Name the blood parasite species.
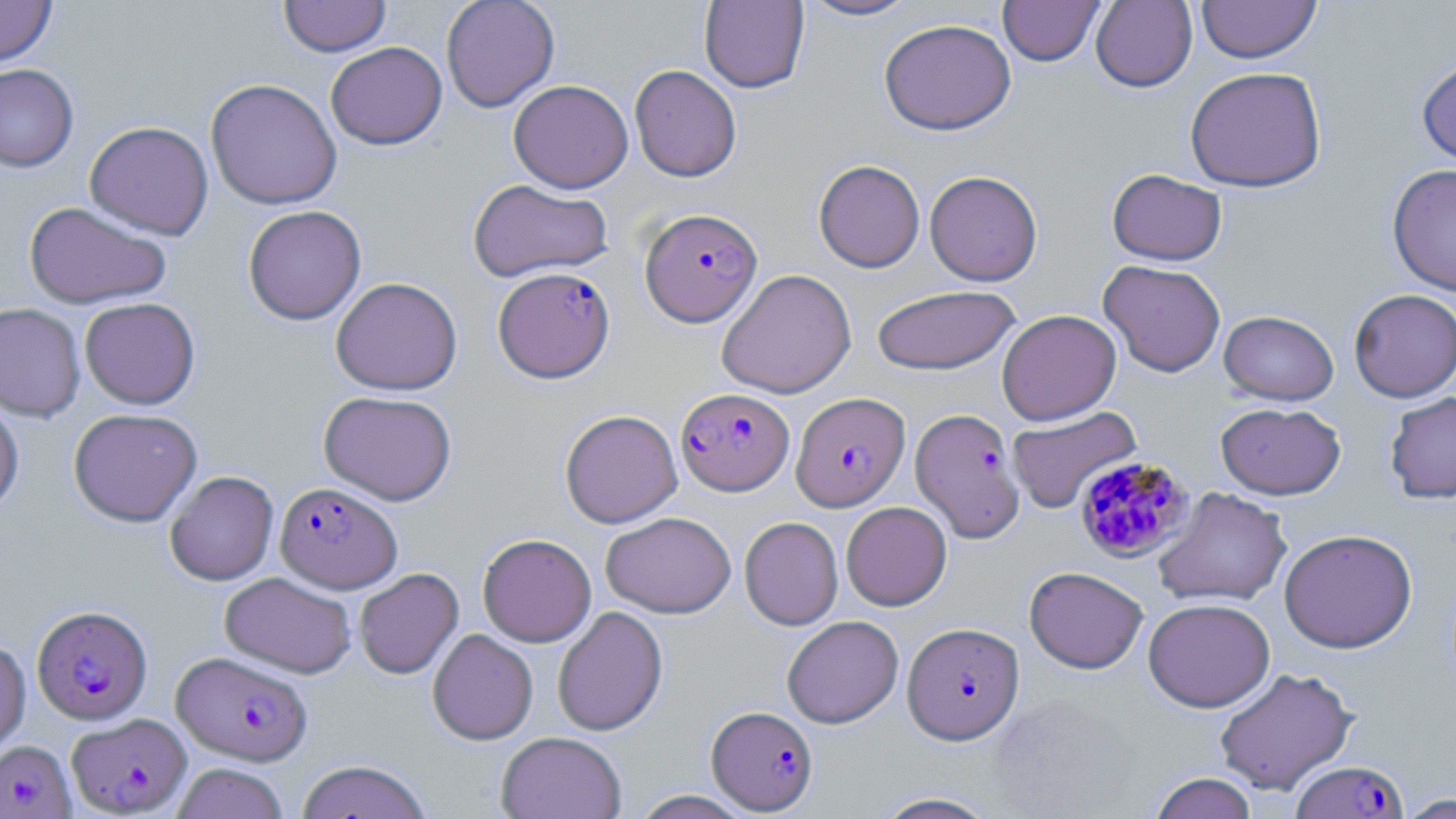

Plasmodium falciparum.

Approximate bounding boxes as (x1, y1, x2, y2) in pixels. Uninfected red blood cell locations: (0, 0, 57, 66), (279, 0, 392, 57), (441, 0, 560, 112), (799, 0, 919, 21), (998, 0, 1105, 65), (1090, 0, 1197, 92), (1197, 0, 1322, 63), (699, 1, 809, 93), (879, 18, 1016, 135), (326, 42, 447, 150), (1416, 54, 1456, 172), (0, 64, 79, 172), (629, 64, 742, 182), (1185, 65, 1328, 192), (205, 78, 342, 210), (508, 80, 633, 193), (84, 121, 214, 240), (814, 159, 925, 272), (1387, 163, 1456, 296), (1107, 169, 1227, 266), (925, 170, 1043, 286), (467, 178, 614, 283), (23, 202, 172, 309), (242, 205, 366, 325), (1098, 260, 1226, 377), (716, 268, 856, 399), (330, 277, 463, 395), (871, 284, 1021, 375), (1349, 288, 1456, 402), (79, 297, 201, 409), (0, 302, 86, 422), (997, 309, 1121, 425), (1219, 310, 1339, 405), (319, 390, 457, 505), (1384, 391, 1456, 504), (0, 393, 24, 517), (1215, 402, 1346, 500), (1006, 406, 1142, 514), (68, 408, 202, 526), (559, 409, 683, 528), (165, 470, 279, 585), (1153, 487, 1292, 608), (841, 501, 952, 611), (600, 511, 737, 618), (739, 516, 843, 630), (1279, 528, 1418, 653), (477, 533, 596, 647), (1024, 566, 1149, 674), (354, 568, 463, 679), (220, 572, 356, 678), (1143, 598, 1275, 712), (552, 606, 668, 736), (781, 615, 903, 728), (428, 629, 538, 745), (0, 639, 31, 757), (1213, 667, 1359, 796), (496, 731, 627, 819), (296, 759, 433, 819), (171, 762, 289, 819), (1148, 772, 1259, 819), (870, 791, 1003, 818), (1395, 793, 1455, 818). Plasmodium falciparum-infected red blood cell locations: (640, 207, 762, 327), (493, 266, 615, 383), (676, 388, 794, 495), (791, 392, 909, 511), (910, 407, 1026, 543), (1073, 455, 1195, 562), (275, 482, 402, 593), (32, 605, 153, 725), (902, 622, 1024, 744), (172, 651, 313, 765), (706, 706, 817, 814), (67, 713, 191, 816), (0, 740, 75, 818), (1291, 759, 1408, 818). Light microscopy. One field of a larger specimen. Thin blood smear. Image is 1456×819 pixels. May-Grünwald-Giemsa stain. Captured at 1000x magnification.